Classify this cell by malaria status.
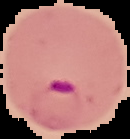

It is parasitized.

image_size: 130×139 pixels
image_type: segmented cell region with the area outside set to black
preparation: thin blood film